Point out each leukocyte.
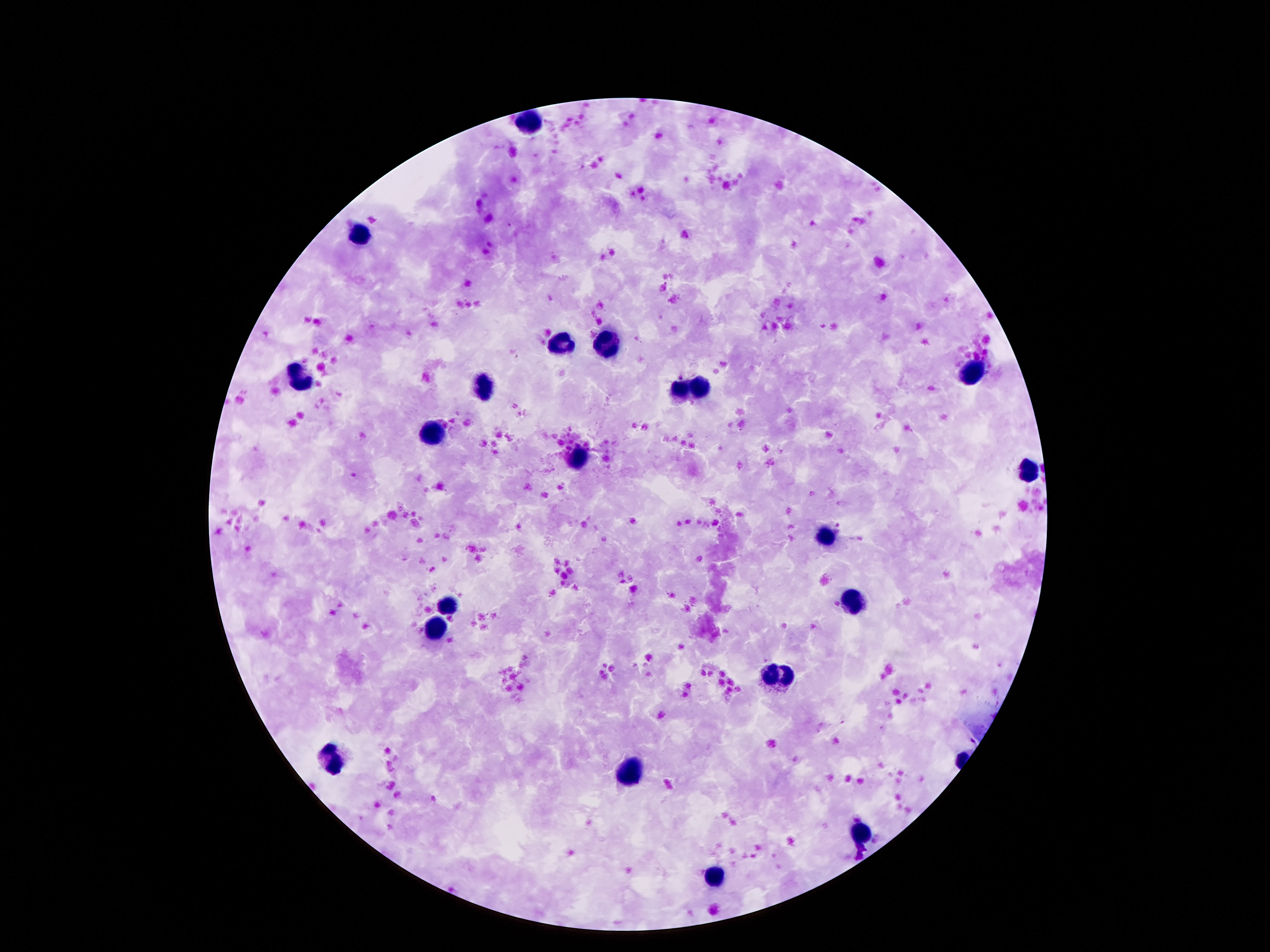
Approximate centers as {x, y} in pixels.
Leukocytes: {530, 122}, {360, 236}, {561, 342}, {606, 345}, {971, 369}, {301, 378}, {485, 388}, {682, 389}, {698, 389}, {434, 437}, {579, 457}, {1028, 471}, {825, 537}, {854, 603}, {448, 605}, {436, 626}, {780, 673}, {329, 755}, {631, 774}, {862, 836}, {713, 878}.

field of view = single
patient malaria status = not infected
capture = smartphone camera through the microscope eyepiece
preparation = thick peripheral-blood smear
magnification = 100x
stain = Giemsa
image size = 1270×952 pixels